Locate every uninfected red blood cell.
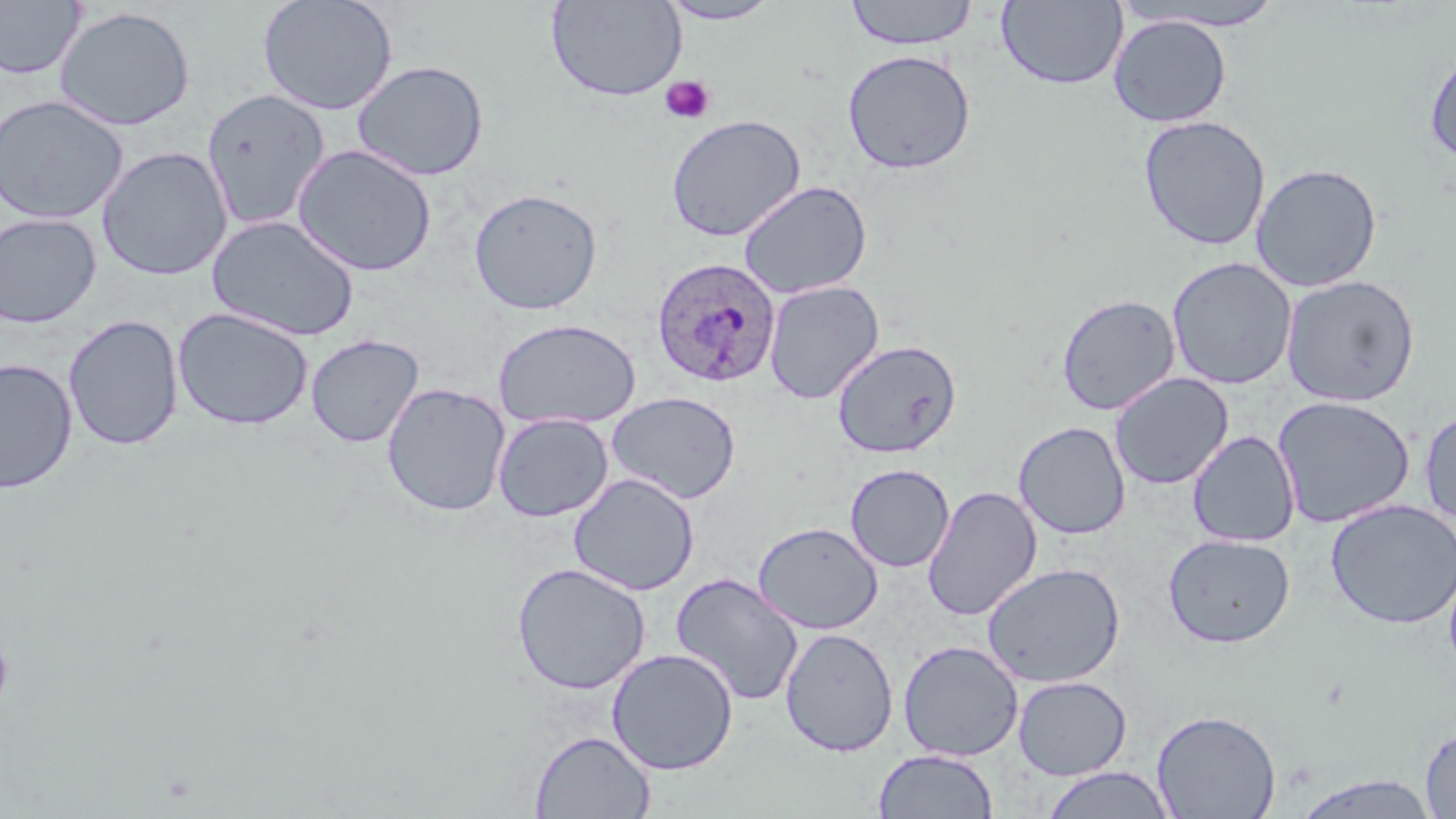

Approximate bounding boxes as (x1, y1, x2, y2) in pixels.
Uninfected red blood cells: (257, 0, 398, 116), (844, 0, 979, 50), (996, 0, 1129, 90), (0, 1, 86, 80), (546, 1, 687, 102), (657, 1, 782, 25), (1121, 2, 1289, 32), (55, 6, 196, 131), (1109, 15, 1232, 127), (1424, 47, 1456, 164), (842, 49, 977, 175), (351, 60, 489, 181), (200, 88, 331, 232), (0, 95, 129, 224), (666, 114, 807, 241), (1138, 115, 1271, 251), (291, 144, 437, 277), (96, 146, 232, 281), (1250, 163, 1383, 292), (738, 180, 872, 299), (468, 187, 603, 315), (0, 212, 102, 328), (207, 214, 360, 342), (1167, 257, 1298, 390), (1280, 274, 1420, 406), (764, 280, 884, 404), (1056, 294, 1181, 415), (172, 307, 314, 431), (62, 314, 184, 452), (492, 318, 642, 430), (305, 334, 424, 447), (832, 339, 962, 458), (0, 357, 78, 494), (1109, 372, 1234, 490), (382, 382, 511, 517), (606, 391, 742, 504), (1272, 395, 1416, 529), (1419, 407, 1456, 528), (492, 412, 614, 522), (1013, 421, 1131, 539), (1187, 430, 1300, 547), (845, 464, 954, 573), (569, 473, 700, 596), (922, 485, 1042, 621), (1325, 499, 1456, 629), (753, 521, 884, 634), (1163, 533, 1295, 648), (1443, 557, 1456, 681), (511, 562, 651, 695), (981, 563, 1125, 687), (670, 572, 804, 707), (780, 627, 899, 757), (898, 641, 1023, 761), (607, 648, 739, 775), (1013, 676, 1132, 780), (1151, 709, 1281, 819), (1420, 724, 1456, 818), (530, 730, 655, 818), (872, 749, 999, 819), (1041, 767, 1177, 819), (1288, 773, 1443, 819).

slide-level diagnosis = Plasmodium ovale
platelet locations = approximate bounding boxes as (x1, y1, x2, y2) in pixels: (660, 75, 715, 124), (0, 634, 14, 715)
image size = 1456×819 pixels
modality = light microscopy
stain = May-Grünwald-Giemsa
Plasmodium ovale-infected red blood cell locations = approximate bounding boxes as (x1, y1, x2, y2) in pixels: (650, 257, 781, 389)
field of view = single
preparation = thin blood film
magnification = 1000x